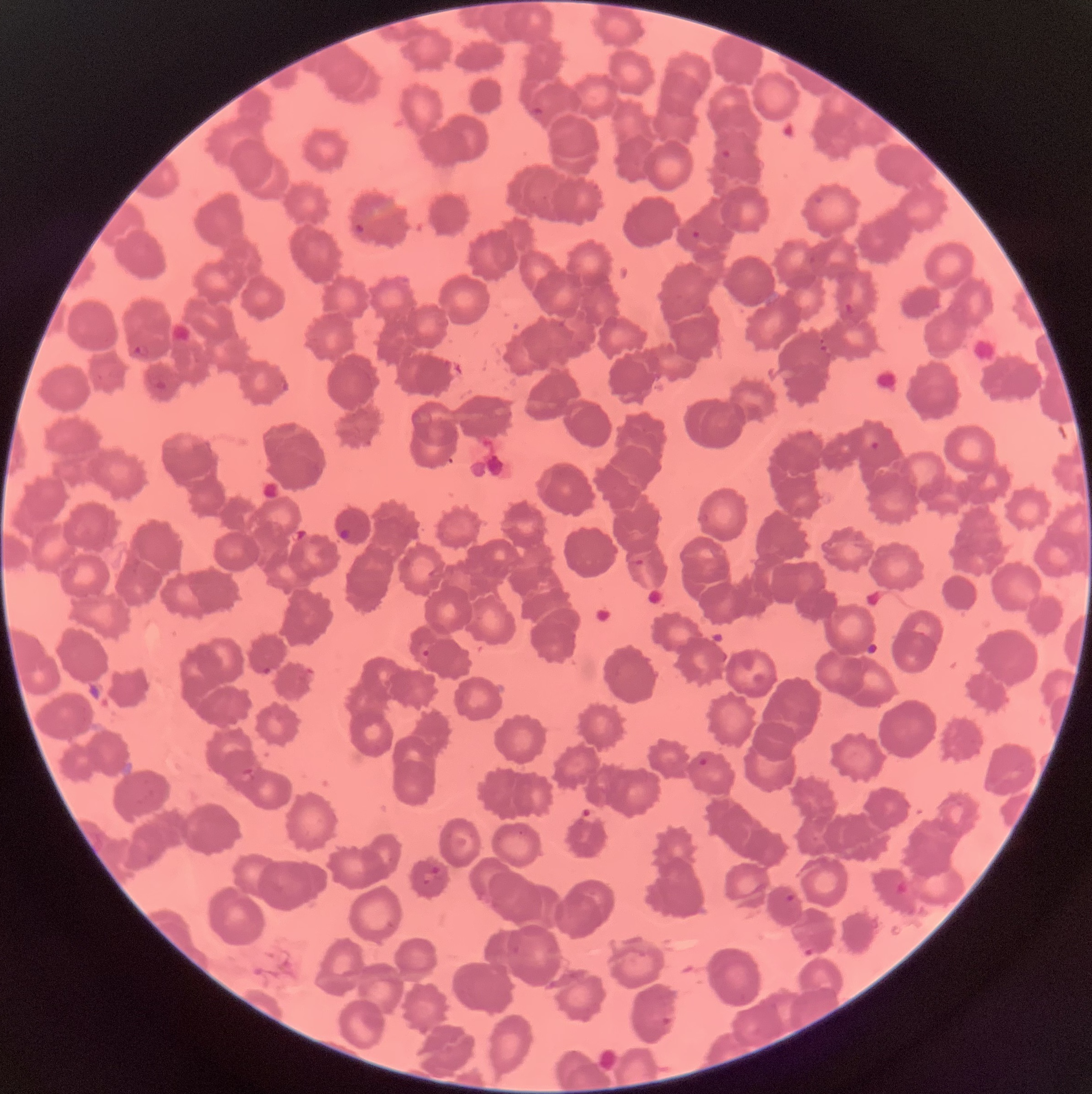
Summary:
  - Coordinate format: approximate bounding boxes as (x1,y1)-(x2,y2) corner pairs in pixels
  - Plasmodium parasite locations: (529,105)-(545,118), (719,148)-(736,161), (813,194)-(825,206), (353,222)-(365,235), (691,229)-(700,240), (807,254)-(819,265), (844,303)-(856,315), (819,337)-(828,353), (132,343)-(149,360), (148,373)-(168,390), (279,379)-(289,392), (863,432)-(881,451), (697,514)-(710,523), (339,527)-(352,541), (635,558)-(644,566), (421,649)-(431,658), (262,666)-(273,675), (698,758)-(709,766), (579,806)-(602,826), (432,865)-(446,881), (422,873)-(432,885), (783,892)-(798,904), (801,946)-(816,957), (659,1015)-(675,1027)
  - Preparation: thin blood film
  - Image size: 1092×1094 pixels
  - Modality: optical microscopy
  - Red blood cell morphology: rouleaux formation